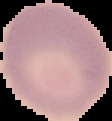
image type = segmented cell region with the area outside set to black
preparation = thin blood smear
result = no Plasmodium parasites detected
image size = 112×121 pixels